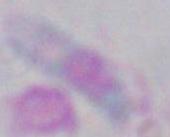
identification = Toxoplasma gondii
magnification = 1000x
modality = photomicrograph